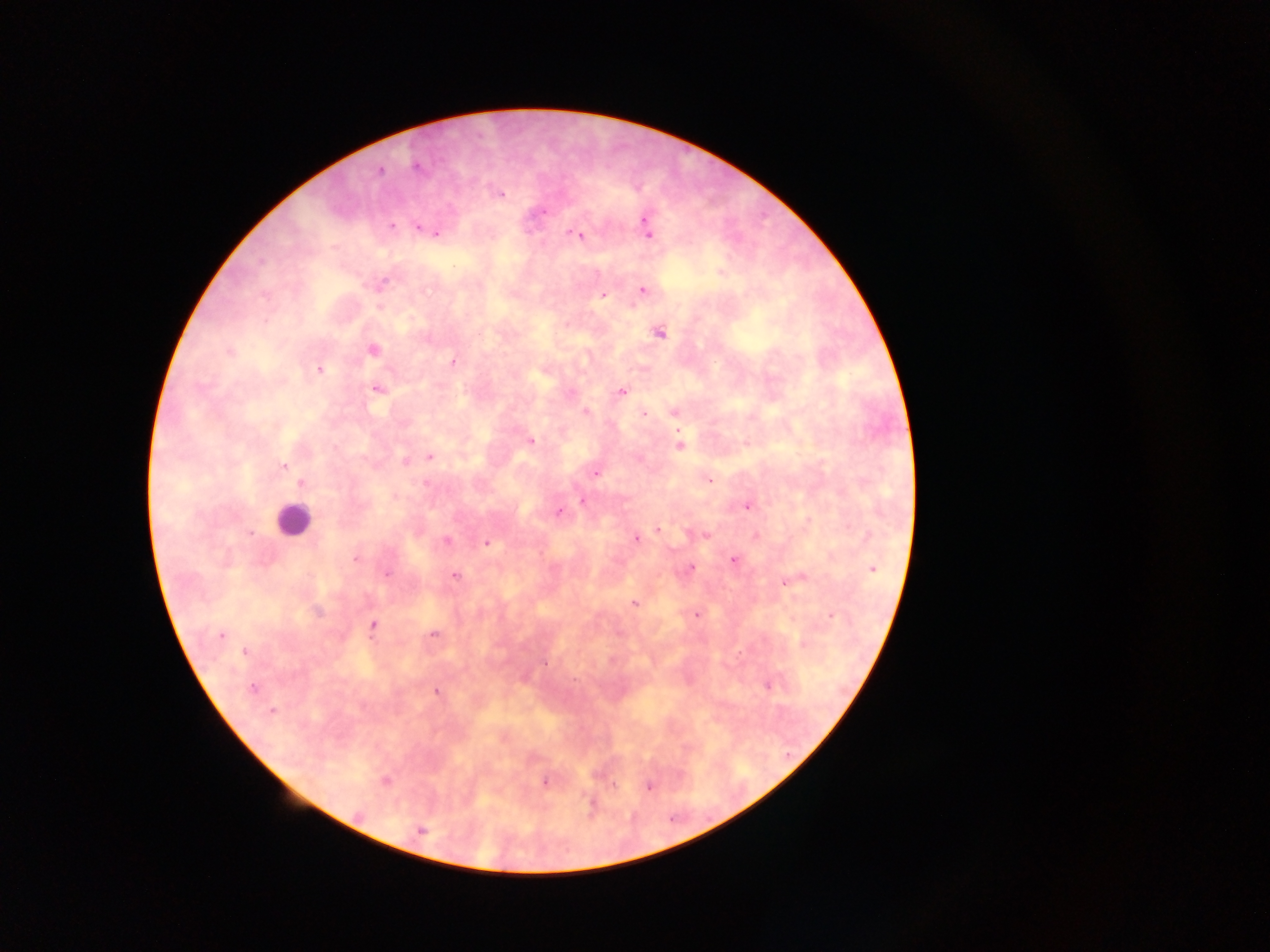

Approximate centers as [x, y] in pixels.
Summary:
  - Plasmodium parasite locations: [416, 167], [380, 171], [501, 193], [392, 227], [418, 227], [647, 229], [437, 233], [579, 236], [383, 284], [642, 291], [265, 295], [603, 295], [661, 333], [372, 349], [230, 352], [452, 362], [319, 370], [377, 389], [622, 391], [585, 412], [675, 412], [644, 414], [531, 441], [679, 445], [430, 457], [405, 461], [284, 466], [595, 474], [709, 480], [301, 483], [426, 483], [583, 501], [747, 506], [558, 512], [657, 529], [251, 533], [704, 534], [636, 539], [446, 541], [486, 544], [356, 558], [734, 560], [690, 569], [872, 569], [386, 573], [456, 576], [796, 579], [785, 582], [635, 603], [317, 612], [696, 615], [832, 615], [372, 625], [434, 634], [221, 635], [245, 652], [545, 664], [767, 686], [253, 688], [436, 691], [271, 712], [385, 780], [545, 783], [614, 786], [649, 787], [591, 806], [358, 815], [421, 831]
  - Leukocyte locations: [293, 520]
  - Country: Ghana
  - Preparation: thick blood smear
  - Field of view: single
  - Image size: 1270×952 pixels
  - Capture: mobile-phone photograph through a microscope